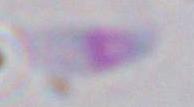
Summary:
  - Modality: micrograph
  - Identification: Toxoplasma gondii
  - Magnification: 1000x